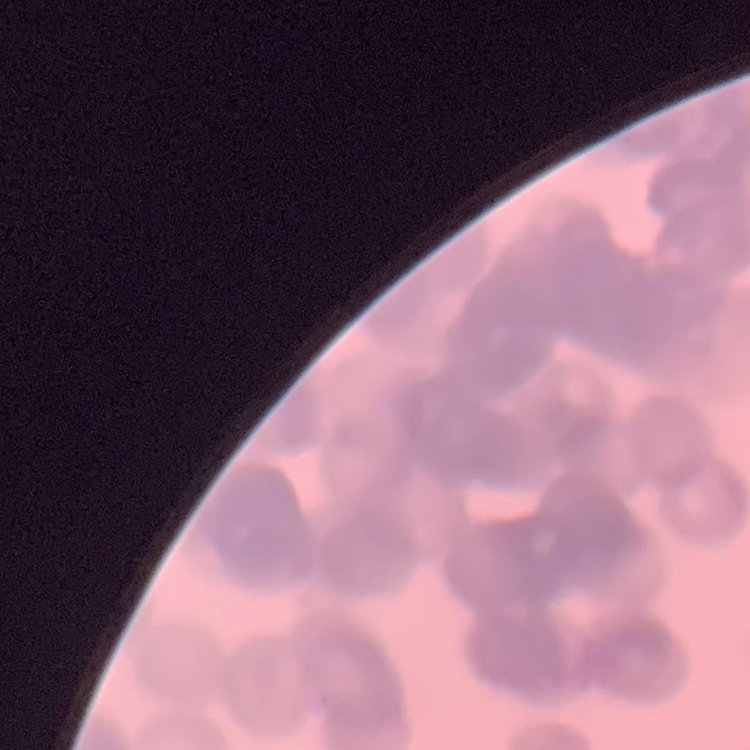 The red blood cells show rouleaux formation. Square crop of a larger photomicrograph. Field's or Giemsa stain. Thin blood film.